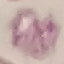

Result: no malaria parasites detected. Giemsa stain. Acquired by smartphone through the microscope eyepiece. Thin blood smear. Automatically extracted cell patch, resized to 64 × 64 pixels.